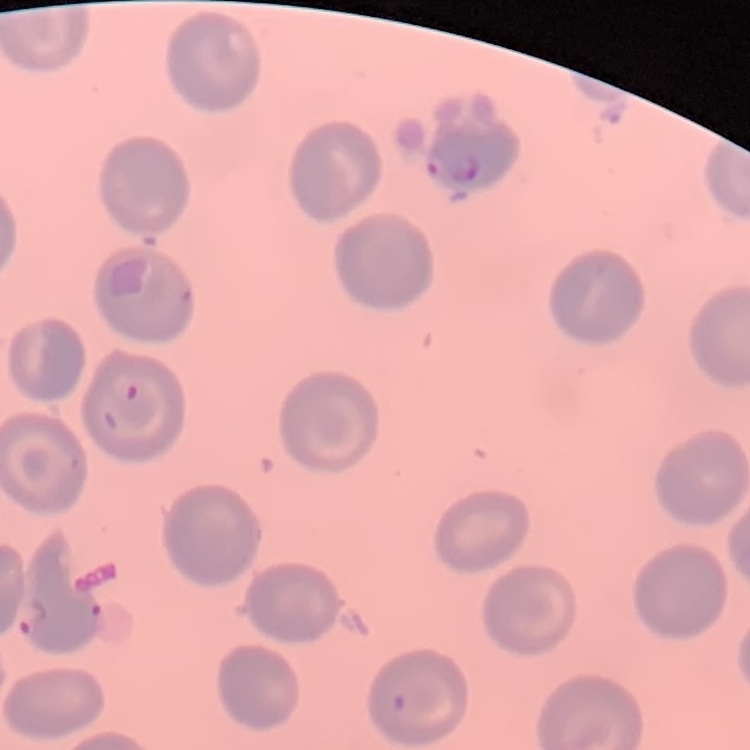

Summary:
  - Red blood cell morphology: no rouleaux formation
  - Image type: square crop of a larger photomicrograph
  - Preparation: thin peripheral smear
  - Stain: Field's or Giemsa